State which parasite is depicted.
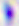

Toxoplasma gondii.

400x magnification. Micrograph.